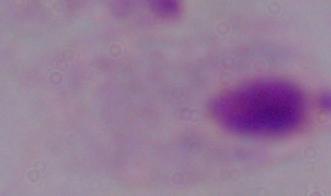 A trichomonad is shown. Photomicrograph. 1000x magnification.